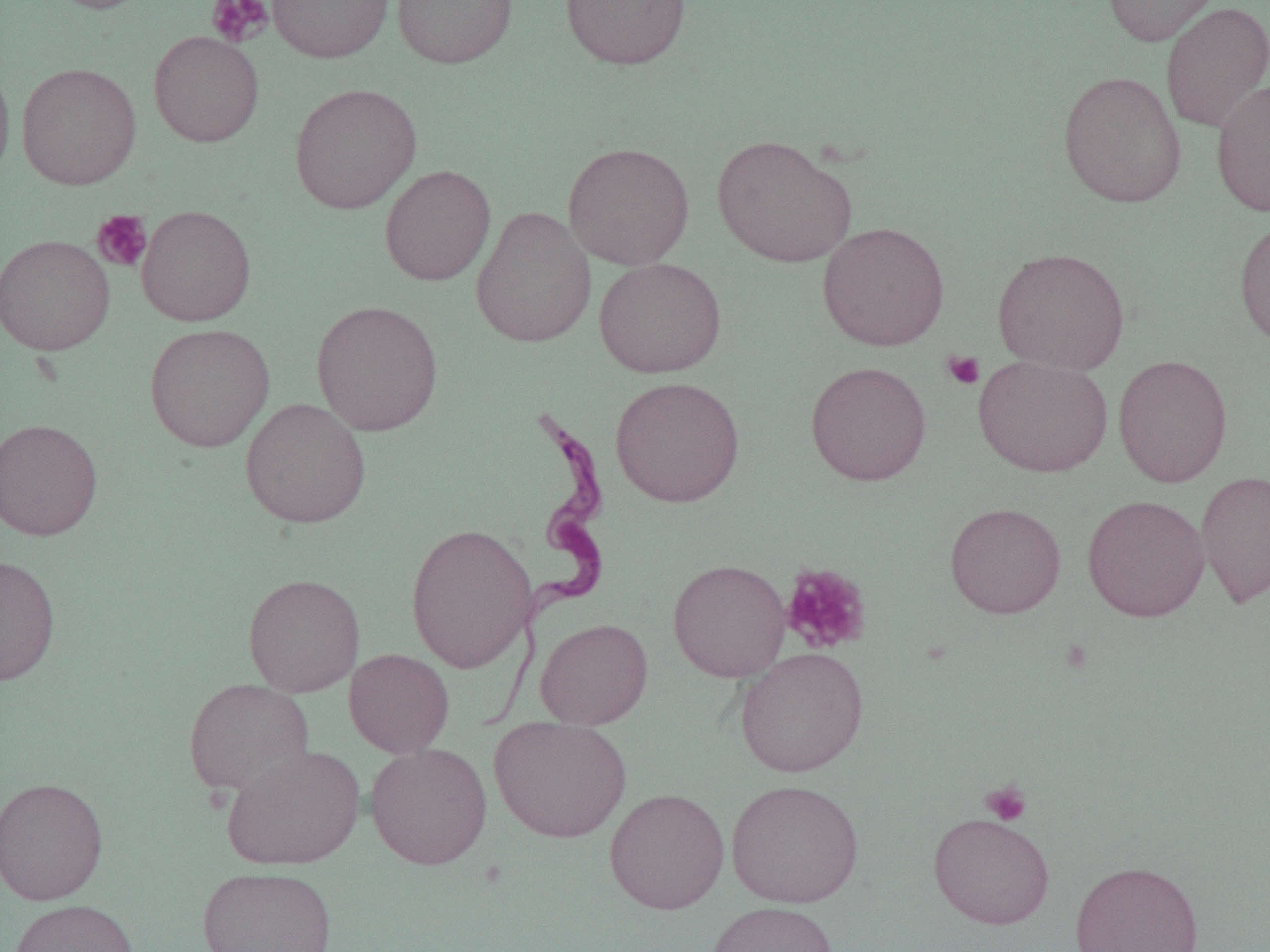

slide_level_diagnosis: Trypanosoma brucei
image_size: 1270×952 pixels
preparation: thin blood smear
magnification: 1000x
trypanosoma_brucei_locations: 'approximate bounding boxes as named x1/y1/x2/y2 corners in pixels: (x1=473, y1=413, x2=616, y2=721)'
modality: optical microscopy
field_of_view: one of a larger specimen
uninfected_red_blood_cell_locations: 'approximate bounding boxes as named x1/y1/x2/y2 corners in pixels: (x1=44, y1=0, x2=157, y2=14), (x1=267, y1=0, x2=393, y2=63), (x1=391, y1=0, x2=518, y2=69), (x1=559, y1=0, x2=691, y2=69), (x1=1102, y1=0, x2=1226, y2=47), (x1=1160, y1=1, x2=1270, y2=134), (x1=148, y1=30, x2=264, y2=147), (x1=0, y1=53, x2=15, y2=184), (x1=16, y1=62, x2=141, y2=190), (x1=1058, y1=71, x2=1187, y2=208), (x1=1211, y1=78, x2=1270, y2=217), (x1=289, y1=83, x2=422, y2=214), (x1=711, y1=133, x2=857, y2=269), (x1=562, y1=141, x2=695, y2=270), (x1=379, y1=164, x2=496, y2=286), (x1=136, y1=205, x2=256, y2=326), (x1=471, y1=206, x2=596, y2=348), (x1=1234, y1=218, x2=1270, y2=349), (x1=817, y1=222, x2=949, y2=351), (x1=0, y1=234, x2=115, y2=355), (x1=992, y1=247, x2=1130, y2=375), (x1=594, y1=258, x2=726, y2=378), (x1=311, y1=300, x2=443, y2=436), (x1=144, y1=323, x2=275, y2=452), (x1=973, y1=354, x2=1113, y2=478), (x1=1113, y1=354, x2=1233, y2=488), (x1=805, y1=360, x2=931, y2=486), (x1=610, y1=376, x2=745, y2=507), (x1=240, y1=397, x2=371, y2=529), (x1=0, y1=418, x2=103, y2=541), (x1=1196, y1=470, x2=1270, y2=608), (x1=1082, y1=494, x2=1210, y2=622), (x1=944, y1=502, x2=1066, y2=618), (x1=405, y1=523, x2=537, y2=673), (x1=0, y1=554, x2=61, y2=686), (x1=667, y1=559, x2=790, y2=682), (x1=242, y1=573, x2=365, y2=697), (x1=535, y1=618, x2=653, y2=728), (x1=735, y1=647, x2=869, y2=778), (x1=344, y1=648, x2=454, y2=757), (x1=184, y1=677, x2=315, y2=796), (x1=489, y1=716, x2=632, y2=843), (x1=365, y1=742, x2=492, y2=870), (x1=221, y1=744, x2=365, y2=871), (x1=0, y1=776, x2=108, y2=906), (x1=725, y1=779, x2=864, y2=908), (x1=604, y1=788, x2=730, y2=914), (x1=928, y1=812, x2=1055, y2=929), (x1=1070, y1=860, x2=1204, y2=952), (x1=197, y1=865, x2=337, y2=952), (x1=8, y1=899, x2=140, y2=952), (x1=704, y1=902, x2=839, y2=952)'
platelet_locations: 'approximate bounding boxes as named x1/y1/x2/y2 corners in pixels: (x1=206, y1=0, x2=273, y2=47), (x1=91, y1=209, x2=153, y2=272), (x1=942, y1=350, x2=985, y2=390), (x1=780, y1=563, x2=872, y2=654), (x1=980, y1=781, x2=1033, y2=826)'